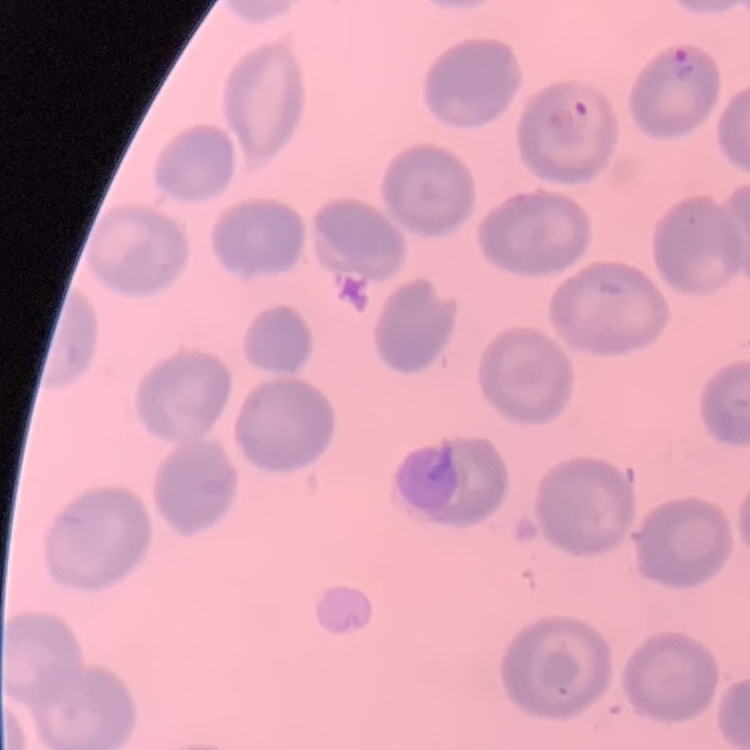
The red blood cells exhibit no rouleaux formation. Stained with either Field's or Giemsa. One tile cut from a larger photomicrograph. Thin blood film.